Assess this cell for malaria.
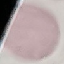

It is uninfected.

Automatically extracted cell patch, resized to 64 × 64 pixels. Acquired by smartphone through the microscope eyepiece. Thin blood film. Giemsa stain.